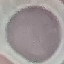

{
  "result": "no malaria parasites detected",
  "stain": "Giemsa",
  "image_type": "automatically extracted cell patch, resized to 64 × 64 pixels",
  "preparation": "thin blood smear",
  "capture": "smartphone camera at the microscope eyepiece"
}